Locate every parasitized red blood cell.
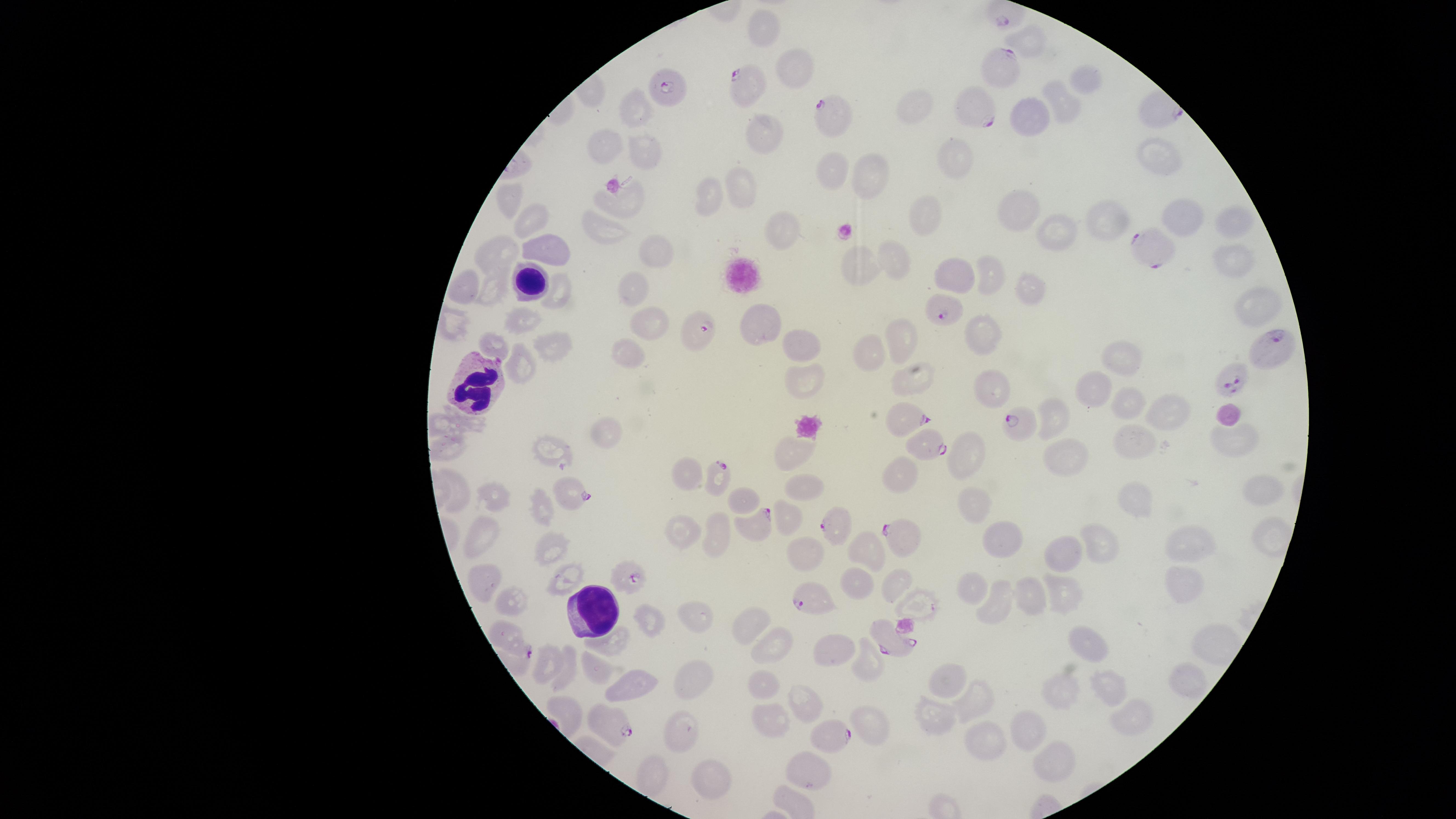

Approximate marker points as {x, y} in pixels.
Parasitized red blood cells: {1000, 61}, {748, 85}, {665, 89}, {974, 110}, {831, 118}, {1153, 246}, {945, 308}, {700, 328}, {1275, 350}, {1229, 383}, {907, 420}, {1019, 423}, {923, 445}, {721, 475}, {574, 492}, {834, 521}, {758, 524}, {902, 537}, {627, 574}, {809, 598}, {893, 644}, {611, 718}, {830, 740}.

{
  "preparation": "thin blood smear",
  "uninfected_red_blood_cells": "approximate marker points as {x, y} in pixels: {764, 25}, {1030, 39}, {794, 70}, {1083, 77}, {1063, 107}, {913, 108}, {636, 109}, {1031, 112}, {763, 134}, {609, 144}, {1160, 154}, {648, 155}, {957, 159}, {838, 168}, {872, 175}, {742, 187}, {713, 193}, {625, 198}, {507, 201}, {1022, 212}, {925, 214}, {1181, 214}, {537, 220}, {1233, 220}, {608, 225}, {1109, 226}, {782, 227}, {1056, 232}, {660, 245}, {500, 250}, {548, 252}, {896, 258}, {1235, 259}, {856, 260}, {960, 275}, {990, 277}, {465, 284}, {632, 285}, {491, 289}, {1022, 289}, {558, 294}, {1255, 303}, {647, 317}, {522, 322}, {755, 324}, {986, 334}, {490, 337}, {901, 338}, {799, 343}, {548, 349}, {868, 352}, {627, 354}, {522, 359}, {1119, 364}, {802, 379}, {915, 382}, {993, 385}, {1098, 390}, {1127, 405}, {1058, 414}, {1166, 414}, {441, 421}, {603, 436}, {1232, 439}, {549, 443}, {1132, 443}, {445, 448}, {794, 451}, {964, 454}, {1067, 455}, {902, 469}, {690, 481}, {803, 486}, {1256, 488}, {745, 497}, {497, 502}, {1143, 503}, {977, 505}, {547, 508}, {789, 517}, {683, 529}, {482, 534}, {719, 534}, {1104, 541}, {1198, 542}, {1003, 544}, {1075, 548}, {557, 549}, {867, 554}, {806, 555}, {573, 574}, {491, 579}, {899, 581}, {856, 582}, {1187, 583}, {1065, 588}, {974, 591}, {1028, 597}, {1003, 599}, {516, 601}, {919, 601}, {699, 614}, {652, 619}, {753, 623}, {1097, 641}, {613, 644}, {778, 651}, {839, 651}, {546, 662}, {568, 663}, {868, 664}, {601, 673}, {1182, 676}, {947, 682}, {692, 686}, {641, 688}, {766, 688}, {1065, 689}, {1106, 689}, {978, 696}, {807, 707}, {567, 709}, {931, 713}, {1132, 715}, {773, 720}, {868, 722}, {1034, 726}, {680, 730}, {986, 740}, {1053, 759}, {811, 771}, {655, 773}, {711, 778}",
  "capture": "smartphone photograph through the microscope eyepiece",
  "visible_region": "circular",
  "image_size": "1456×819 pixels",
  "stain": "Giemsa",
  "species": "Plasmodium falciparum",
  "white_blood_cells": "approximate marker points as {x, y} in pixels: {533, 282}, {476, 385}, {596, 605}",
  "field_of_view": "single"
}